Outline white blood cells.
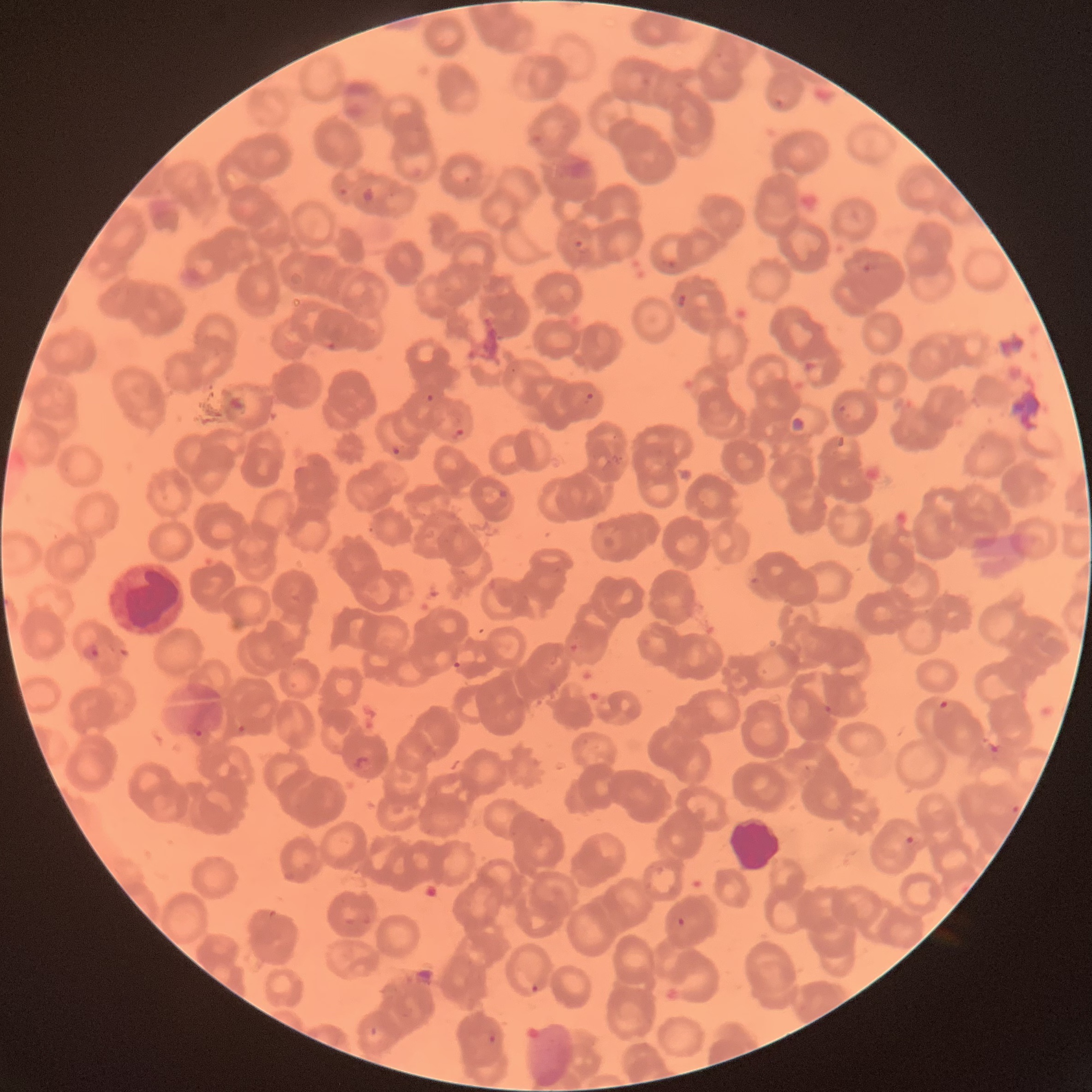
Approximate bounding boxes as (x1, y1, x2, y2) in pixels.
White blood cells: (105, 560, 186, 636), (729, 816, 782, 872).

Summary:
  - Plasmodium parasite locations: (572, 238, 591, 253), (663, 257, 679, 271), (861, 260, 878, 273), (674, 289, 688, 307), (322, 336, 337, 352), (800, 358, 818, 375), (580, 391, 595, 405), (424, 392, 435, 403), (838, 403, 847, 415), (451, 426, 466, 440), (389, 444, 403, 458), (497, 488, 508, 500), (81, 642, 101, 663), (451, 659, 463, 670), (937, 699, 950, 711), (822, 703, 832, 714), (193, 730, 205, 739), (353, 753, 371, 772), (1009, 803, 1022, 815), (903, 834, 915, 846), (676, 916, 687, 929), (527, 982, 541, 995), (485, 1032, 499, 1046)
  - Modality: light microscopy
  - Preparation: thin blood smear
  - Red blood cell morphology: rouleaux formation
  - Image size: 1092×1092 pixels